Locate every uninfected red blood cell.
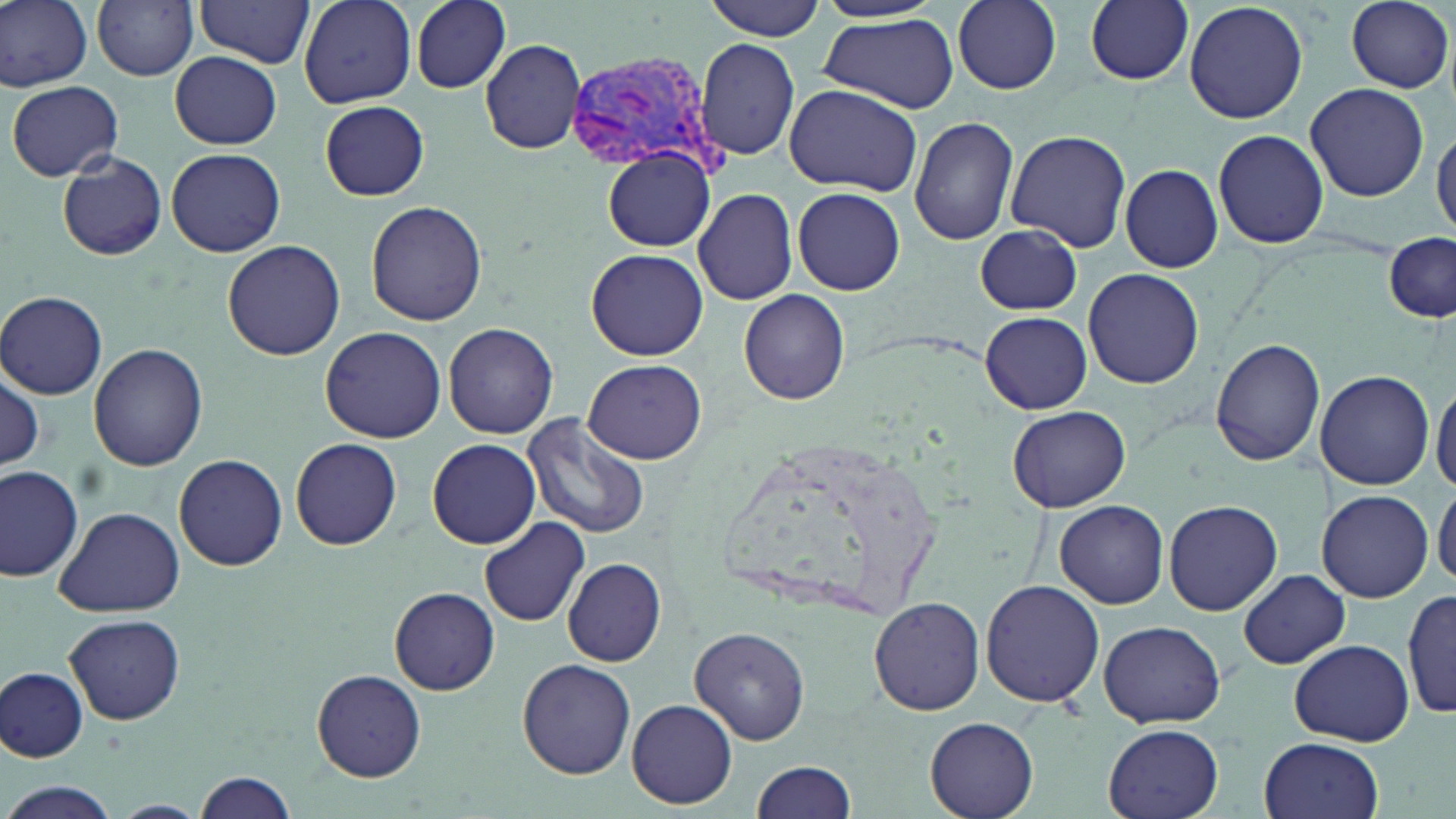

Approximate bounding boxes as named x1/y1/x2/y2 corners in pixels.
Uninfected red blood cells: (x1=0, y1=0, x2=94, y2=91), (x1=196, y1=0, x2=314, y2=70), (x1=298, y1=0, x2=417, y2=108), (x1=411, y1=0, x2=510, y2=92), (x1=703, y1=0, x2=827, y2=41), (x1=954, y1=0, x2=1062, y2=93), (x1=1084, y1=0, x2=1193, y2=86), (x1=1345, y1=0, x2=1453, y2=93), (x1=92, y1=1, x2=200, y2=80), (x1=1182, y1=1, x2=1309, y2=125), (x1=818, y1=16, x2=959, y2=112), (x1=481, y1=37, x2=586, y2=155), (x1=696, y1=38, x2=799, y2=161), (x1=169, y1=51, x2=281, y2=149), (x1=7, y1=79, x2=124, y2=182), (x1=1304, y1=82, x2=1430, y2=203), (x1=784, y1=83, x2=922, y2=197), (x1=319, y1=99, x2=430, y2=201), (x1=909, y1=115, x2=1018, y2=247), (x1=1432, y1=124, x2=1456, y2=241), (x1=1211, y1=129, x2=1328, y2=249), (x1=1004, y1=131, x2=1131, y2=252), (x1=165, y1=147, x2=286, y2=257), (x1=603, y1=149, x2=715, y2=253), (x1=57, y1=151, x2=167, y2=260), (x1=1119, y1=163, x2=1224, y2=273), (x1=693, y1=187, x2=798, y2=305), (x1=791, y1=187, x2=905, y2=295), (x1=365, y1=202, x2=487, y2=326), (x1=972, y1=225, x2=1084, y2=316), (x1=1382, y1=232, x2=1456, y2=322), (x1=222, y1=240, x2=345, y2=360), (x1=587, y1=247, x2=708, y2=361), (x1=1083, y1=267, x2=1204, y2=390), (x1=738, y1=289, x2=851, y2=405), (x1=0, y1=290, x2=109, y2=399), (x1=979, y1=310, x2=1092, y2=414), (x1=443, y1=322, x2=558, y2=439), (x1=319, y1=327, x2=447, y2=441), (x1=1210, y1=338, x2=1325, y2=466), (x1=88, y1=344, x2=208, y2=471), (x1=582, y1=359, x2=705, y2=464), (x1=0, y1=369, x2=45, y2=473), (x1=1316, y1=370, x2=1434, y2=491), (x1=1430, y1=380, x2=1456, y2=496), (x1=1003, y1=404, x2=1131, y2=512), (x1=521, y1=415, x2=651, y2=539), (x1=289, y1=437, x2=403, y2=550), (x1=426, y1=437, x2=541, y2=549), (x1=174, y1=454, x2=289, y2=571), (x1=0, y1=466, x2=83, y2=583), (x1=1433, y1=482, x2=1456, y2=591), (x1=1317, y1=490, x2=1432, y2=603), (x1=1164, y1=499, x2=1283, y2=615), (x1=1053, y1=501, x2=1169, y2=609), (x1=53, y1=507, x2=185, y2=618), (x1=480, y1=517, x2=589, y2=626), (x1=563, y1=557, x2=666, y2=668), (x1=1238, y1=570, x2=1350, y2=669), (x1=981, y1=578, x2=1104, y2=709), (x1=390, y1=587, x2=501, y2=694), (x1=1403, y1=589, x2=1455, y2=722), (x1=868, y1=596, x2=984, y2=717), (x1=65, y1=613, x2=186, y2=725), (x1=1098, y1=619, x2=1225, y2=727), (x1=690, y1=626, x2=811, y2=745), (x1=1288, y1=638, x2=1413, y2=747), (x1=518, y1=659, x2=636, y2=778), (x1=1, y1=666, x2=89, y2=762), (x1=312, y1=669, x2=426, y2=782), (x1=626, y1=698, x2=736, y2=808), (x1=925, y1=716, x2=1038, y2=819), (x1=1103, y1=723, x2=1226, y2=819), (x1=1259, y1=737, x2=1383, y2=819), (x1=751, y1=759, x2=859, y2=819), (x1=192, y1=771, x2=298, y2=818), (x1=5, y1=783, x2=116, y2=818), (x1=109, y1=800, x2=211, y2=819).

Plasmodium vivax-infected red blood cell locations = approximate bounding boxes as named x1/y1/x2/y2 corners in pixels: (x1=568, y1=51, x2=722, y2=178)
slide-level diagnosis = Plasmodium vivax
preparation = thin blood film
field of view = single
modality = light microscopy
magnification = 1000x
image size = 1456×819 pixels
stain = May-Grünwald-Giemsa